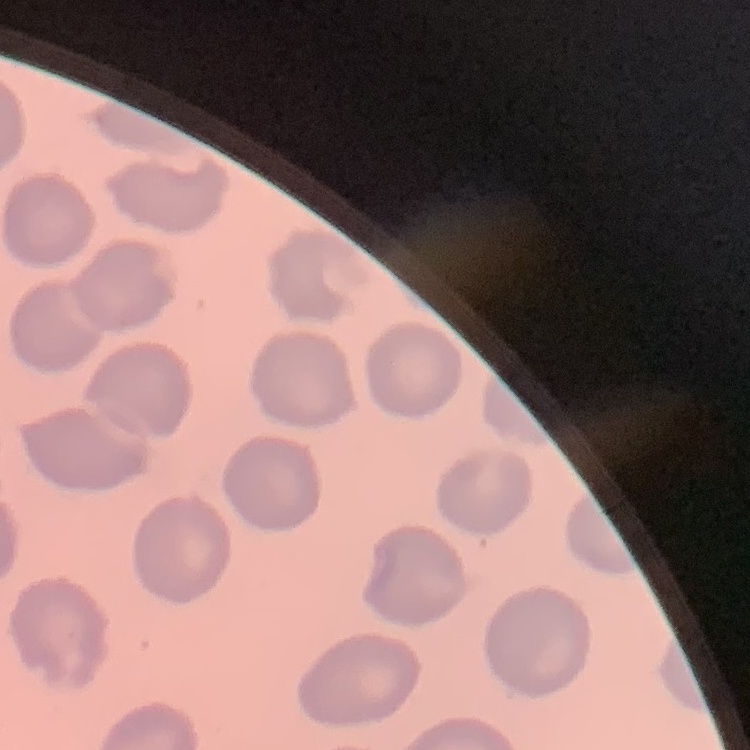
erythrocyte_morphology: no rouleaux formation
image_type: square crop of a larger photomicrograph
preparation: thin blood film
stain: Field's or Giemsa